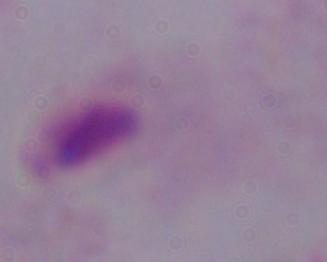
Summary:
  - Modality: micrograph
  - Identification: trichomonad
  - Magnification: 1000x